Assess this cell for malaria.
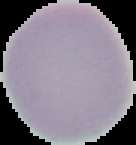
Uninfected.

image type = segmented cell region on a black background
image size = 136×145 pixels
preparation = thin blood film